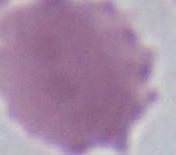
Summary:
  - Identification: red blood cell
  - Magnification: 1000x
  - Modality: micrograph